Identify the parasite.
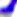

This is Toxoplasma gondii.

magnification = 400x
modality = micrograph